Outline every Plasmodium parasite, every leukocyte, and every artifact (stain precipitate or debris).
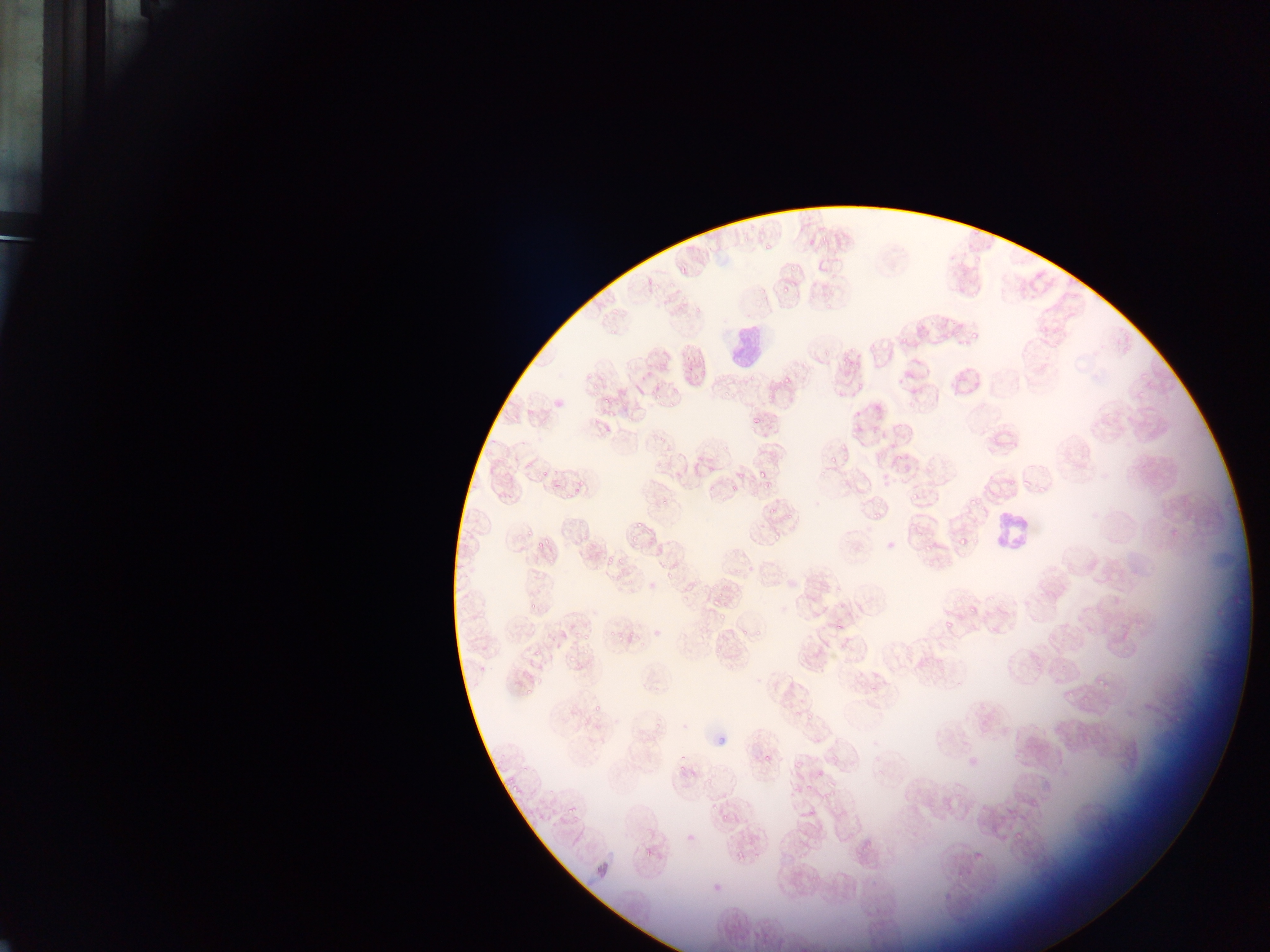

Approximate bounding boxes as left top right bottom in pixels.
Plasmodium parasites: 809 239 817 248; 779 281 793 294; 962 327 987 345; 780 375 792 393; 603 395 612 405; 748 416 760 428; 848 416 860 433; 825 453 839 469; 757 464 772 482; 734 470 742 481; 1019 473 1033 487; 728 485 737 495; 907 489 923 501; 963 490 978 510; 763 495 785 518; 869 509 881 523; 624 527 640 541; 770 533 782 543; 960 537 969 546; 536 540 548 552; 921 544 932 554; 662 570 672 582; 711 598 723 609; 966 602 978 613; 736 613 757 639; 714 614 731 621; 941 616 959 631; 831 617 851 636; 526 646 549 660; 565 653 576 671; 515 669 543 687; 1091 675 1109 696; 1060 680 1083 701; 524 685 541 699; 589 698 600 718; 569 699 582 726; 587 722 604 745; 761 753 769 765; 815 769 824 778; 568 805 579 816; 1012 827 1026 845; 685 832 695 841; 643 847 652 858; 729 850 750 863.
Leukocytes: 726 322 763 366; 992 516 1033 554.

Summary:
  - Capture: mobile-phone photograph through a microscope
  - Field of view: single
  - Country: Ghana
  - Image size: 1270×952 pixels
  - Preparation: thin blood film